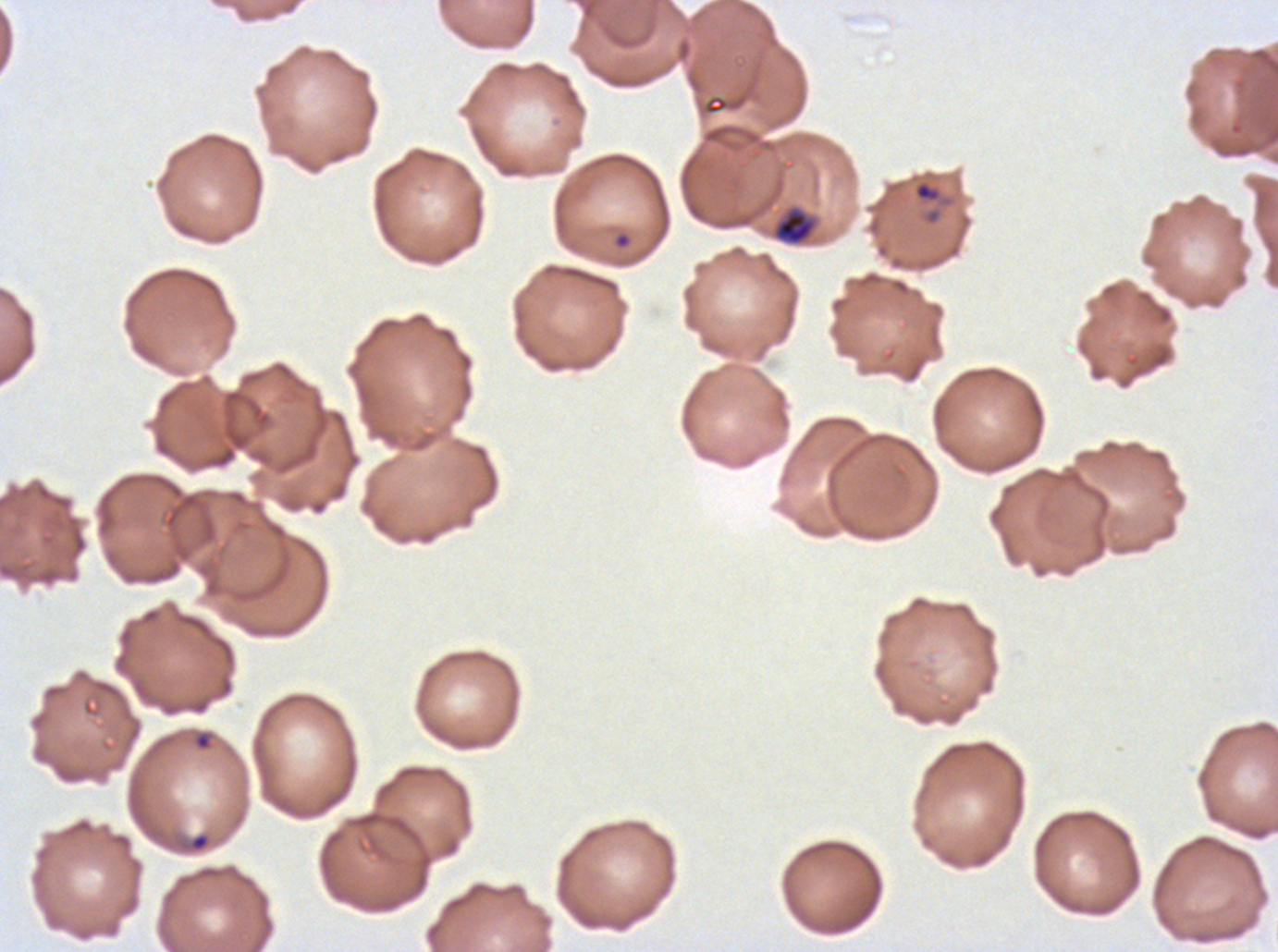

{
  "ring_locations": "approximate bounding boxes as [x1, y1, x2, y2] in pixels: [912, 178, 954, 208], [612, 231, 632, 250], [193, 732, 212, 751], [188, 832, 211, 853]",
  "late_ring_early_trophozoite_locations": "approximate bounding boxes as [x1, y1, x2, y2] in pixels: [776, 212, 813, 244]",
  "life_cycle_stages_observed": "ring, late-ring/early-trophozoite",
  "field_of_view": "sub-image separated from a larger composite",
  "preparation": "thin blood film",
  "specimen": "ex-vivo Plasmodium falciparum culture from a patient in The Gambia, grown for 24 to 48 hours",
  "stain": "Giemsa",
  "image_size": "1278×952 pixels"
}